Comment on the morphology of the erythrocytes.
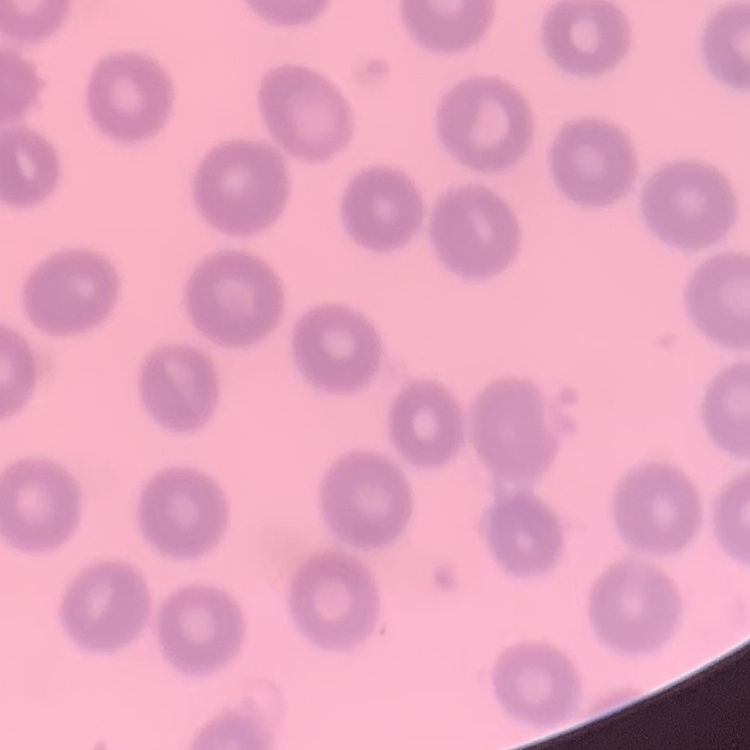
They show no rouleaux formation.

Summary:
  - Stain: Field's or Giemsa
  - Preparation: thin peripheral smear
  - Image type: square crop of a larger photomicrograph